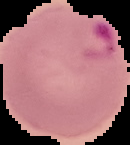

image type = segmented cell region with the area outside set to black
malaria status = parasitized
image size = 130×145 pixels
preparation = thin blood smear